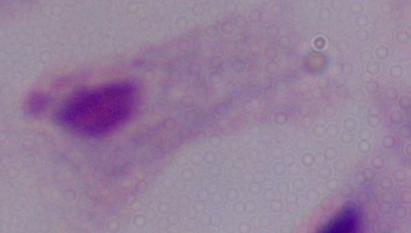
A trichomonad is seen. 1000x magnification. Photomicrograph.